Identify the parasite.
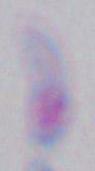
This is Toxoplasma gondii.

modality = photomicrograph
magnification = 1000x